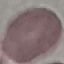 Malaria status: uninfected. Acquired by smartphone through the microscope eyepiece. Giemsa stain. Thin smear of blood. Automatically extracted cell patch, resized to 64 × 64 pixels.